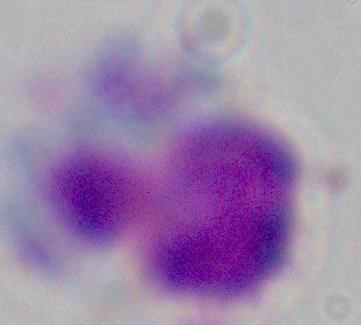

magnification = 1000x
modality = photomicrograph
identification = white blood cell